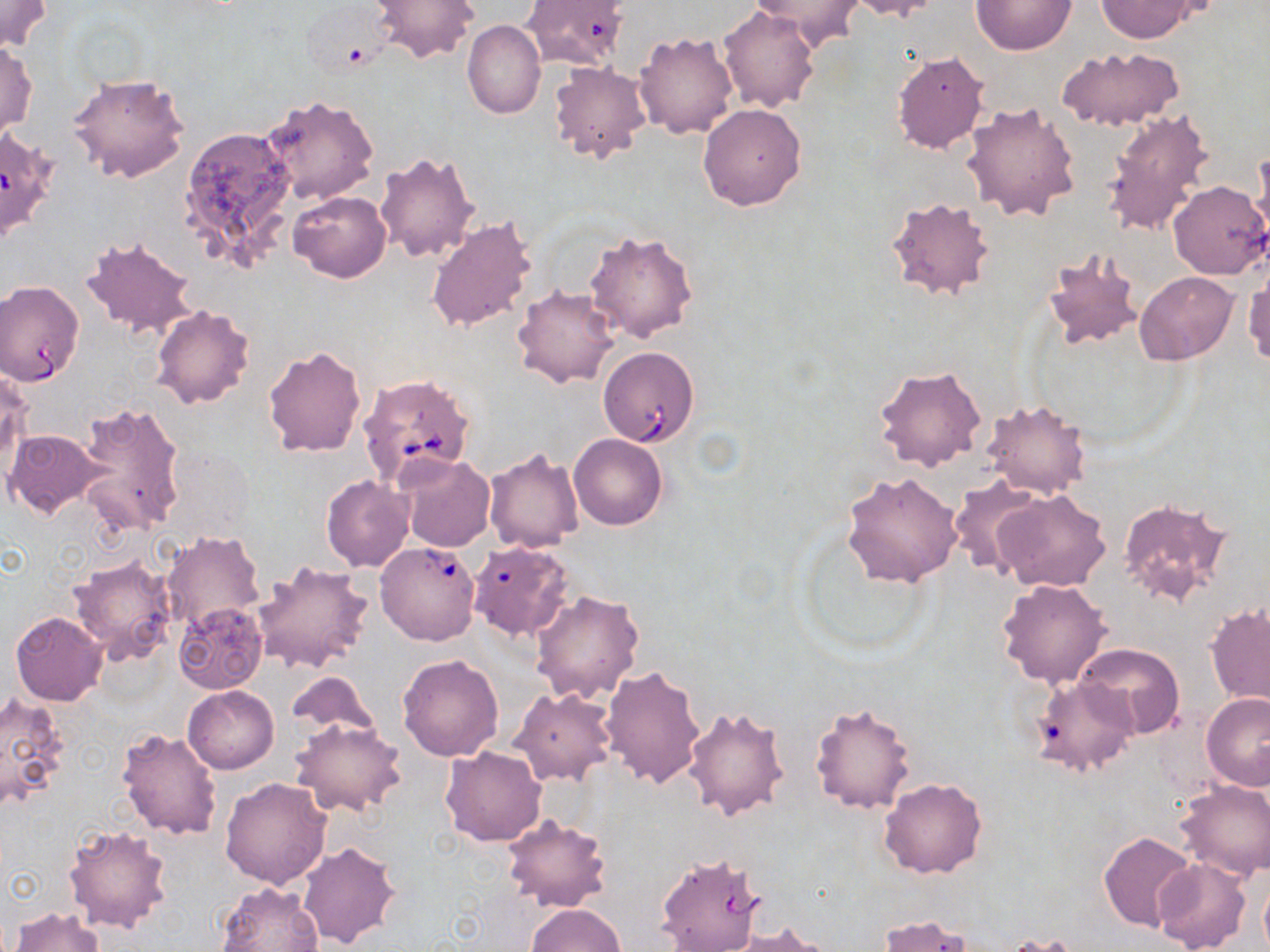
Summary:
  - Coordinate format: approximate bounding boxes as [x1, y1, x2, y2] in pixels
  - Babesia divergens-infected red blood cell locations: [0, 281, 85, 385], [598, 346, 699, 447], [358, 373, 477, 487], [375, 541, 481, 646]
  - Uninfected red blood cell locations: [371, 0, 479, 64], [520, 0, 630, 70], [746, 0, 866, 47], [848, 0, 943, 21], [971, 0, 1077, 54], [1097, 0, 1195, 41], [0, 2, 52, 52], [719, 6, 819, 112], [462, 20, 545, 118], [634, 30, 739, 139], [0, 43, 38, 137], [1055, 46, 1184, 133], [891, 51, 988, 153], [548, 62, 650, 164], [68, 72, 190, 183], [262, 95, 379, 206], [961, 101, 1082, 223], [697, 103, 807, 210], [1104, 108, 1217, 231], [179, 124, 297, 265], [375, 150, 481, 263], [1250, 152, 1270, 251], [1167, 181, 1267, 279], [289, 190, 391, 283], [886, 195, 997, 301], [426, 216, 538, 336], [584, 228, 700, 343], [81, 234, 199, 340], [1042, 247, 1143, 349], [1244, 266, 1270, 370], [1135, 271, 1239, 364], [511, 284, 622, 390], [151, 305, 255, 408], [262, 344, 366, 458], [873, 363, 987, 473], [1, 368, 32, 473], [980, 398, 1092, 499], [74, 400, 187, 537], [4, 429, 108, 517], [569, 432, 669, 529], [484, 448, 584, 553], [396, 455, 496, 552], [842, 471, 962, 588], [321, 476, 414, 572], [948, 477, 1044, 577], [992, 488, 1111, 592], [1116, 494, 1234, 608], [162, 531, 264, 631], [469, 547, 572, 640], [66, 554, 178, 669], [251, 560, 374, 673], [996, 577, 1114, 689], [531, 588, 645, 704], [1205, 601, 1270, 709], [175, 603, 266, 694], [11, 611, 107, 706], [1074, 642, 1184, 739], [397, 653, 505, 761], [599, 665, 706, 789], [284, 672, 382, 748], [1036, 679, 1136, 776], [183, 685, 280, 774], [509, 686, 617, 786], [0, 690, 70, 812], [1201, 692, 1270, 789], [809, 699, 917, 812], [682, 703, 791, 821], [290, 717, 409, 819], [117, 727, 222, 840], [440, 746, 546, 846], [219, 776, 331, 889], [878, 777, 988, 878], [1175, 779, 1270, 882], [500, 814, 611, 913], [62, 823, 174, 933], [1097, 831, 1198, 932], [297, 840, 400, 950], [1152, 859, 1250, 952], [216, 881, 323, 952], [527, 903, 625, 952], [9, 908, 105, 952], [877, 915, 977, 952], [720, 923, 838, 951], [999, 934, 1082, 952]
  - Slide-level diagnosis: Babesia divergens
  - Preparation: thin blood film
  - Image size: 1270×952 pixels
  - Stain: May-Grünwald-Giemsa
  - Modality: light microscopy
  - Magnification: 1000x
  - Field of view: single